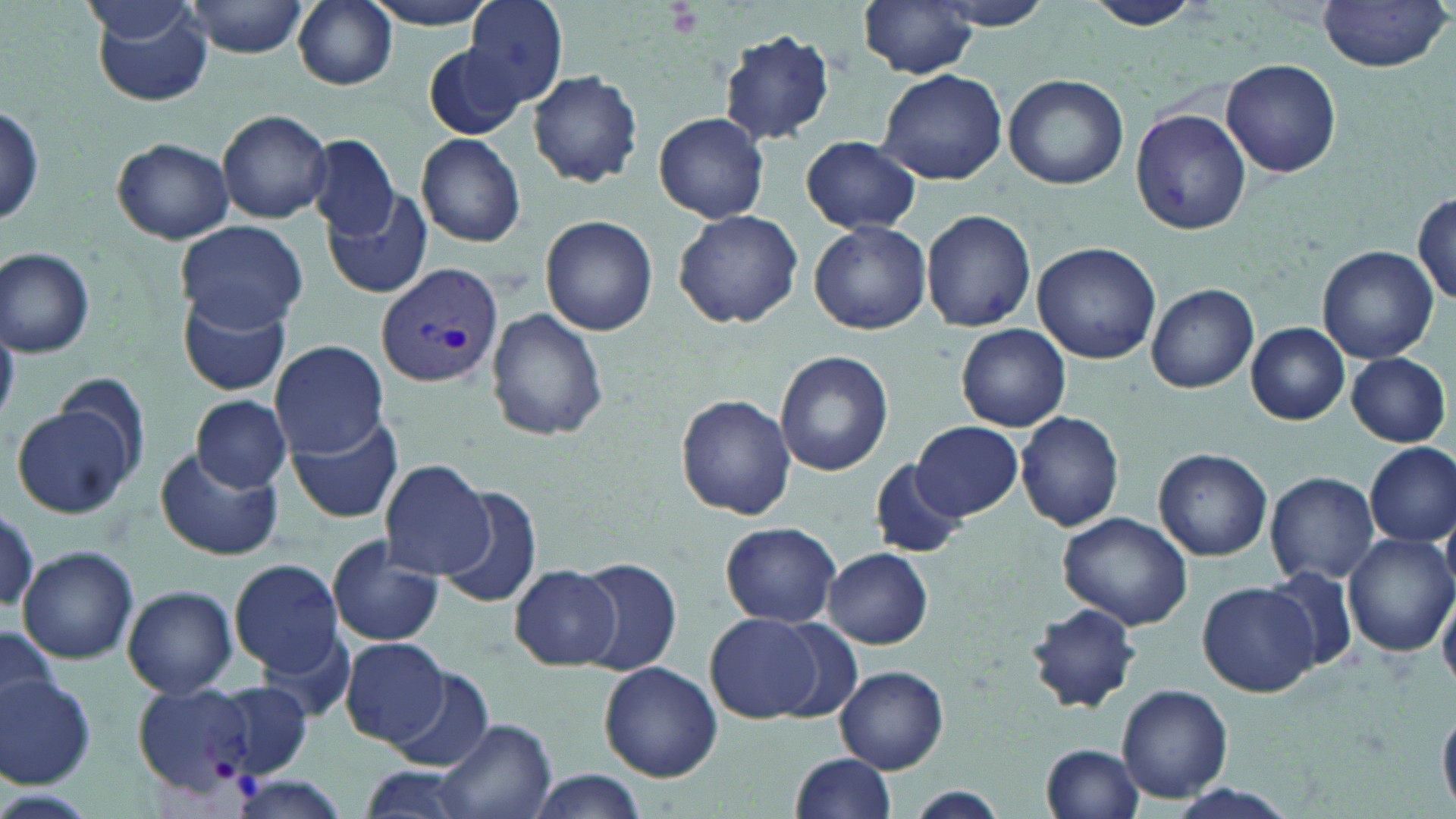
Summary:
  - Coordinate format: approximate bounding boxes as (x1,y1)-(x2,y2) corner pairs in pixels
  - Uninfected red blood cell locations: (183,0)-(309,58), (293,0)-(398,90), (358,0)-(506,30), (462,0)-(570,109), (859,0)-(980,78), (926,0)-(1060,30), (1085,0)-(1206,32), (91,1)-(216,108), (1318,1)-(1451,72), (716,30)-(837,145), (421,42)-(528,142), (1220,58)-(1341,179), (876,67)-(1008,185), (527,70)-(644,187), (1004,74)-(1130,189), (0,107)-(46,229), (1131,108)-(1251,235), (218,109)-(336,222), (654,111)-(770,223), (416,134)-(527,248), (305,135)-(401,237), (801,136)-(922,234), (112,137)-(235,243), (322,185)-(433,299), (1413,191)-(1456,305), (673,208)-(803,330), (921,208)-(1036,332), (539,214)-(658,336), (177,220)-(306,331), (808,220)-(932,334), (1033,241)-(1161,363), (1317,245)-(1438,363), (1,247)-(96,358), (1144,284)-(1259,394), (177,292)-(292,399), (486,308)-(607,438), (1246,323)-(1350,425), (956,324)-(1070,432), (270,339)-(389,458), (775,350)-(893,476), (1345,351)-(1451,447), (57,372)-(150,468), (192,395)-(292,492), (676,395)-(795,518), (9,405)-(137,519), (1014,410)-(1125,532), (286,412)-(402,527), (913,420)-(1022,520), (1364,442)-(1456,549), (153,447)-(285,562), (1154,448)-(1272,561), (869,458)-(968,560), (381,460)-(497,580), (1264,470)-(1381,584), (433,485)-(543,607), (1057,512)-(1195,630), (720,521)-(841,629), (1346,533)-(1455,658), (326,537)-(445,647), (18,545)-(138,664), (822,547)-(934,649), (576,557)-(683,677), (228,558)-(343,678), (510,564)-(623,671), (1264,566)-(1360,673), (1198,582)-(1319,697), (123,585)-(238,698), (1439,585)-(1456,687), (1025,603)-(1140,714), (703,612)-(830,722), (0,629)-(60,722), (340,637)-(448,747), (598,662)-(723,783), (382,665)-(497,772), (835,665)-(948,773), (0,675)-(97,789), (212,683)-(314,778), (1117,685)-(1232,802), (1439,705)-(1456,810), (433,717)-(557,819), (1040,744)-(1144,819), (791,753)-(899,819), (351,766)-(481,819), (523,770)-(652,818), (227,777)-(352,819), (898,787)-(1016,817)
  - Plasmodium vivax-infected red blood cell locations: (377,262)-(505,390), (131,682)-(268,795)
  - Slide-level diagnosis: Plasmodium vivax
  - Image size: 1456×819 pixels
  - Modality: light microscopy
  - Stain: May-Grünwald-Giemsa
  - Field of view: single
  - Magnification: 1000x
  - Preparation: thin blood smear